Identify the blood parasite species.
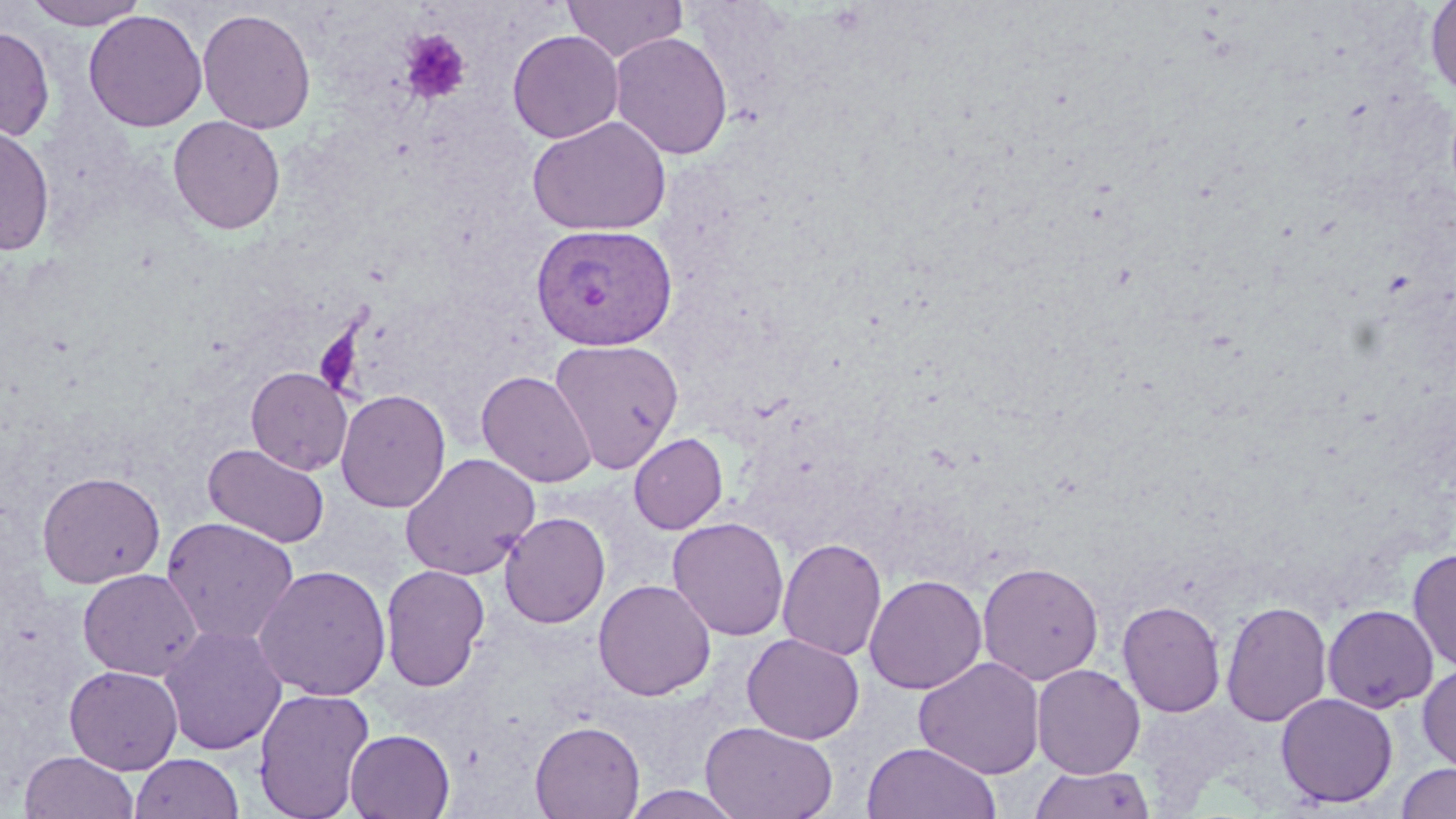
Plasmodium vivax.

{
  "platelet_locations": "approximate bounding boxes as [x1, y1, x2, y2] in pixels: [400, 29, 472, 105]",
  "stain": "May-Grünwald-Giemsa",
  "magnification": "1000x",
  "modality": "light microscopy",
  "field_of_view": "one of a larger specimen",
  "plasmodium_vivax_infected_red_blood_cell_locations": "approximate bounding boxes as [x1, y1, x2, y2] in pixels: [529, 223, 678, 351]",
  "uninfected_red_blood_cell_locations": "approximate bounding boxes as [x1, y1, x2, y2] in pixels: [23, 0, 151, 29], [562, 0, 687, 62], [1424, 0, 1456, 98], [197, 7, 316, 134], [84, 9, 207, 132], [0, 25, 55, 141], [507, 29, 624, 143], [609, 31, 733, 160], [168, 115, 286, 235], [527, 116, 671, 237], [0, 124, 55, 257], [548, 338, 684, 473], [246, 367, 353, 475], [477, 370, 597, 487], [336, 389, 450, 512], [629, 433, 727, 533], [203, 443, 330, 548], [400, 453, 539, 580], [37, 471, 165, 588], [499, 512, 611, 628], [161, 516, 300, 647], [668, 516, 789, 641], [777, 537, 887, 661], [1407, 547, 1456, 673], [977, 561, 1104, 685], [254, 564, 392, 700], [380, 564, 490, 691], [78, 568, 203, 681], [864, 574, 987, 694], [593, 579, 716, 701], [1117, 600, 1225, 718], [1221, 600, 1333, 728], [1322, 604, 1439, 713], [159, 624, 287, 755], [742, 633, 864, 744], [914, 657, 1045, 779], [1417, 663, 1456, 772], [1032, 664, 1145, 779], [64, 665, 183, 774], [253, 687, 374, 819], [1276, 692, 1398, 808], [530, 720, 645, 818], [700, 721, 838, 819], [344, 728, 455, 819], [861, 742, 1001, 819], [19, 751, 139, 819], [130, 753, 244, 819], [1395, 762, 1456, 819], [1030, 764, 1154, 819], [620, 786, 746, 819]",
  "preparation": "thin blood film",
  "image_size": "1456×819 pixels"
}